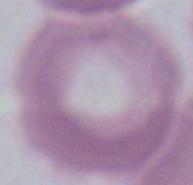

Summary:
  - Magnification: 1000x
  - Modality: photomicrograph
  - Identification: erythrocyte